Assess this cell for malaria.
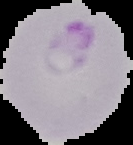
Parasitized.

Image is 133×145 pixels. Segmented cell region on a black background. From a thin blood film.